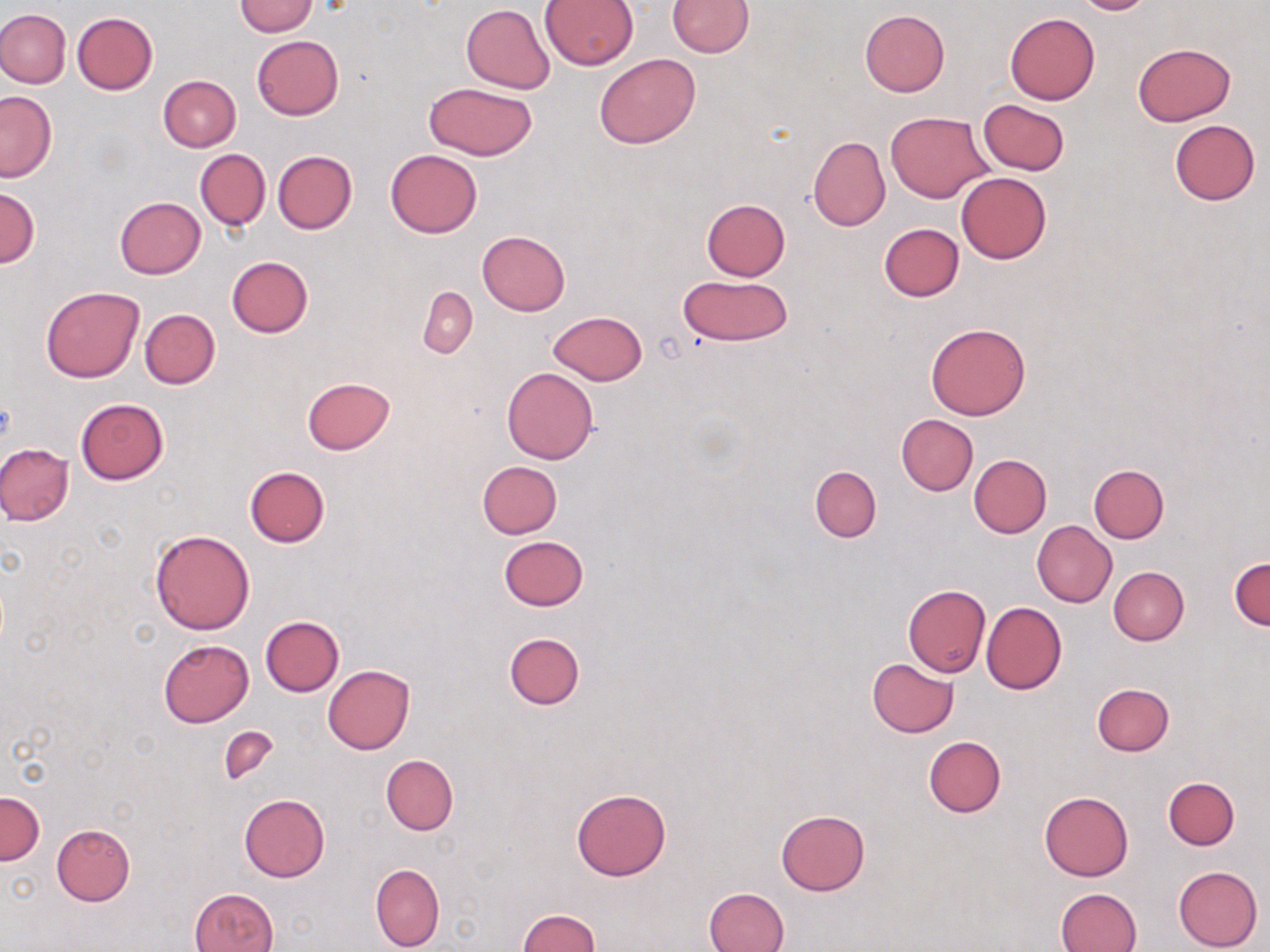
Approximate bounding boxes as named x1/y1/x2/y2 corners in pixels. Uninfected red blood cell locations: (x1=668, y1=0, x2=754, y2=56), (x1=1070, y1=0, x2=1157, y2=15), (x1=232, y1=1, x2=318, y2=36), (x1=540, y1=1, x2=639, y2=68), (x1=461, y1=4, x2=554, y2=93), (x1=0, y1=9, x2=70, y2=88), (x1=858, y1=9, x2=950, y2=97), (x1=72, y1=12, x2=158, y2=94), (x1=1005, y1=13, x2=1099, y2=104), (x1=251, y1=35, x2=344, y2=120), (x1=1132, y1=42, x2=1236, y2=125), (x1=595, y1=52, x2=699, y2=148), (x1=159, y1=76, x2=240, y2=152), (x1=423, y1=81, x2=539, y2=161), (x1=1, y1=91, x2=56, y2=182), (x1=979, y1=99, x2=1069, y2=176), (x1=885, y1=112, x2=991, y2=202), (x1=1169, y1=119, x2=1260, y2=206), (x1=807, y1=135, x2=890, y2=232), (x1=196, y1=149, x2=270, y2=230), (x1=385, y1=150, x2=481, y2=239), (x1=272, y1=151, x2=357, y2=234), (x1=957, y1=172, x2=1051, y2=263), (x1=0, y1=186, x2=39, y2=268), (x1=115, y1=196, x2=205, y2=278), (x1=702, y1=199, x2=791, y2=280), (x1=878, y1=223, x2=964, y2=302), (x1=477, y1=231, x2=570, y2=316), (x1=226, y1=256, x2=314, y2=338), (x1=677, y1=275, x2=792, y2=347), (x1=40, y1=286, x2=144, y2=382), (x1=418, y1=286, x2=477, y2=358), (x1=139, y1=308, x2=220, y2=388), (x1=548, y1=310, x2=647, y2=384), (x1=925, y1=322, x2=1031, y2=420), (x1=502, y1=367, x2=599, y2=464), (x1=302, y1=377, x2=396, y2=455), (x1=75, y1=398, x2=169, y2=484), (x1=896, y1=414, x2=978, y2=496), (x1=0, y1=441, x2=74, y2=526), (x1=969, y1=454, x2=1051, y2=537), (x1=477, y1=461, x2=562, y2=538), (x1=1089, y1=464, x2=1169, y2=543), (x1=245, y1=465, x2=331, y2=547), (x1=809, y1=465, x2=882, y2=541), (x1=1032, y1=521, x2=1117, y2=607), (x1=149, y1=528, x2=255, y2=635), (x1=499, y1=536, x2=588, y2=611), (x1=1230, y1=556, x2=1270, y2=630), (x1=1108, y1=567, x2=1188, y2=646), (x1=902, y1=585, x2=990, y2=677), (x1=981, y1=602, x2=1066, y2=694), (x1=259, y1=617, x2=344, y2=696), (x1=504, y1=632, x2=585, y2=710), (x1=159, y1=639, x2=254, y2=726), (x1=867, y1=658, x2=958, y2=737), (x1=322, y1=665, x2=416, y2=754), (x1=1090, y1=683, x2=1174, y2=756), (x1=220, y1=726, x2=280, y2=786), (x1=924, y1=735, x2=1006, y2=817), (x1=382, y1=755, x2=457, y2=834), (x1=1163, y1=778, x2=1239, y2=850), (x1=571, y1=788, x2=672, y2=881), (x1=0, y1=791, x2=44, y2=865), (x1=1039, y1=791, x2=1133, y2=881), (x1=239, y1=794, x2=330, y2=881), (x1=775, y1=810, x2=870, y2=895), (x1=51, y1=823, x2=136, y2=906), (x1=370, y1=862, x2=444, y2=952), (x1=1173, y1=865, x2=1263, y2=951), (x1=704, y1=886, x2=790, y2=952), (x1=1056, y1=887, x2=1142, y2=952), (x1=190, y1=888, x2=278, y2=952), (x1=518, y1=910, x2=602, y2=952). Slide-level diagnosis: no evidence of blood parasites. One field of a larger specimen. Image is 1270×952 pixels. Optical microscopy. 1000x magnification. Thin blood smear. May-Grünwald-Giemsa-stained preparation.